Assess the morphology of the erythrocytes.
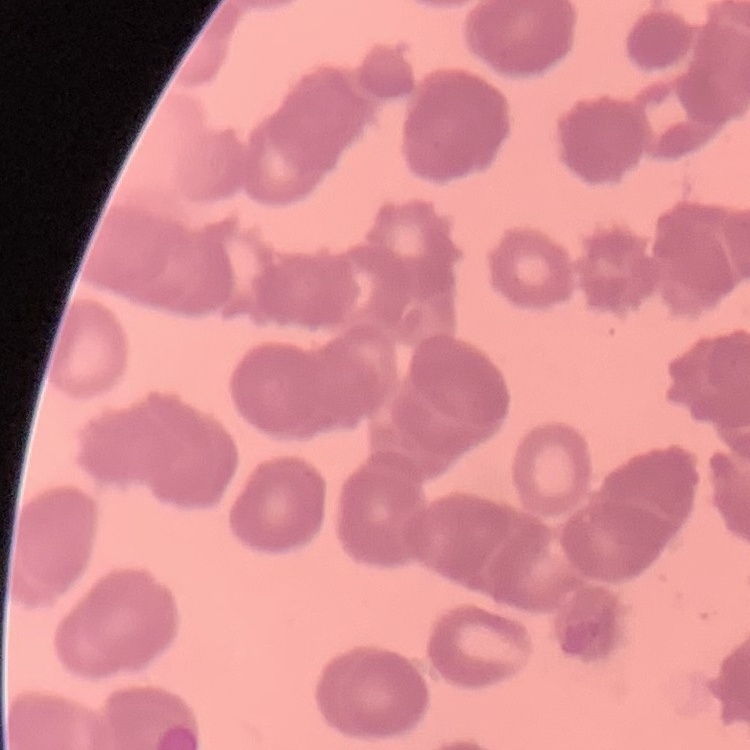

They show rouleaux formation.

Stained with either Field's or Giemsa. Thin peripheral smear. One tile cut from a larger photomicrograph.